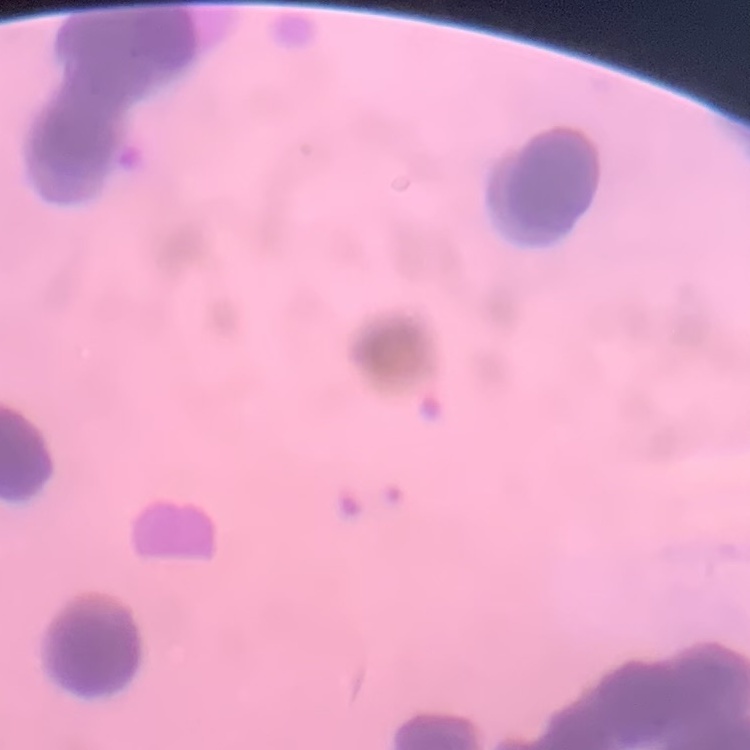

The red blood cells exhibit rouleaux formation. Square crop of a larger photomicrograph. Field's or Giemsa stain. Thin blood smear.